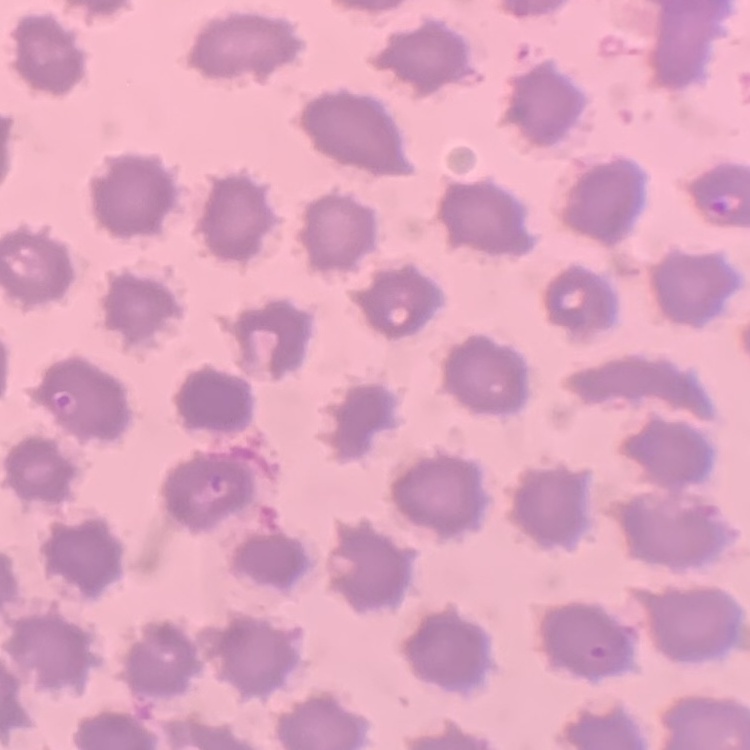

red blood cell morphology = no rouleaux formation
image type = one tile cut from a larger photomicrograph
preparation = thin peripheral smear
stain = Field's or Giemsa